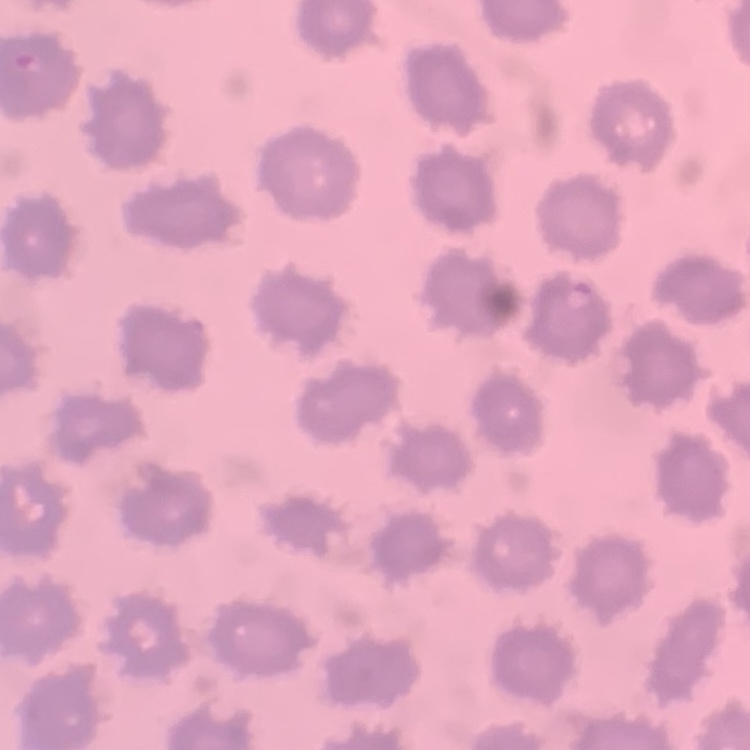

The red blood cells show no rouleaux formation. Field's or Giemsa stain. One tile cut from a larger photomicrograph. Thin blood film.